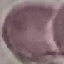

Result: no malaria parasites detected. Giemsa-stained preparation. Acquired by smartphone through the microscope eyepiece. Cell patch, automatically extracted from a larger field of view and resized to 64 × 64 pixels. Thin blood smear.